Locate and identify every blood parasite.
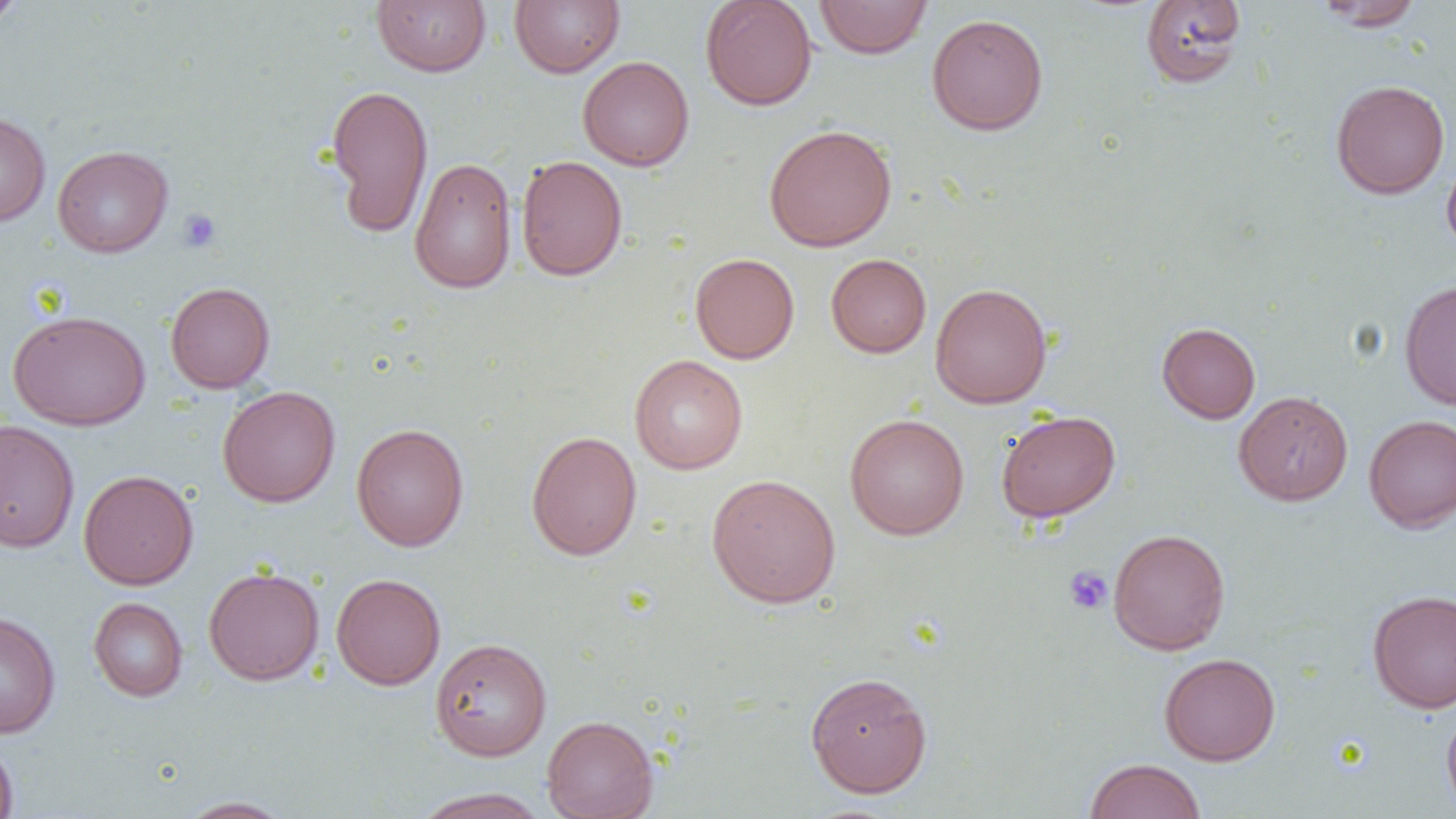

No blood parasites seen.

Summary:
  - Coordinate format: approximate bounding boxes as named x1/y1/x2/y2 corners in pixels
  - Uninfected red blood cell locations: (x1=0, y1=0, x2=27, y2=30), (x1=509, y1=0, x2=624, y2=78), (x1=700, y1=0, x2=818, y2=111), (x1=814, y1=0, x2=932, y2=59), (x1=372, y1=1, x2=491, y2=76), (x1=1141, y1=1, x2=1246, y2=89), (x1=1313, y1=1, x2=1424, y2=31), (x1=927, y1=13, x2=1048, y2=136), (x1=577, y1=56, x2=694, y2=172), (x1=1331, y1=79, x2=1450, y2=199), (x1=325, y1=84, x2=433, y2=238), (x1=0, y1=110, x2=51, y2=227), (x1=764, y1=124, x2=897, y2=251), (x1=52, y1=145, x2=174, y2=257), (x1=1442, y1=153, x2=1456, y2=257), (x1=516, y1=155, x2=628, y2=281), (x1=409, y1=157, x2=517, y2=294), (x1=689, y1=252, x2=800, y2=364), (x1=826, y1=253, x2=931, y2=358), (x1=1399, y1=279, x2=1456, y2=410), (x1=165, y1=281, x2=275, y2=393), (x1=930, y1=283, x2=1052, y2=408), (x1=8, y1=310, x2=151, y2=431), (x1=1156, y1=322, x2=1261, y2=424), (x1=629, y1=354, x2=747, y2=474), (x1=217, y1=386, x2=341, y2=507), (x1=1233, y1=390, x2=1353, y2=506), (x1=996, y1=410, x2=1120, y2=522), (x1=844, y1=413, x2=969, y2=540), (x1=1363, y1=414, x2=1456, y2=533), (x1=0, y1=419, x2=80, y2=553), (x1=351, y1=423, x2=469, y2=551), (x1=525, y1=430, x2=642, y2=560), (x1=78, y1=470, x2=198, y2=590), (x1=706, y1=473, x2=841, y2=608), (x1=1107, y1=528, x2=1231, y2=655), (x1=203, y1=566, x2=324, y2=685), (x1=331, y1=573, x2=446, y2=690), (x1=1367, y1=588, x2=1456, y2=713), (x1=88, y1=597, x2=188, y2=701), (x1=0, y1=611, x2=61, y2=738), (x1=430, y1=638, x2=552, y2=761), (x1=1159, y1=652, x2=1281, y2=765), (x1=805, y1=670, x2=933, y2=798), (x1=1441, y1=705, x2=1456, y2=819), (x1=542, y1=715, x2=658, y2=819), (x1=0, y1=737, x2=19, y2=819), (x1=1085, y1=758, x2=1205, y2=819), (x1=412, y1=788, x2=549, y2=819), (x1=175, y1=796, x2=296, y2=818)
  - Platelet locations: (x1=177, y1=208, x2=222, y2=253), (x1=1063, y1=566, x2=1113, y2=615)
  - Slide-level diagnosis: no evidence of blood parasites
  - Image size: 1456×819 pixels
  - Preparation: thin blood smear
  - Field of view: one of a larger specimen
  - Magnification: 1000x
  - Modality: light microscopy